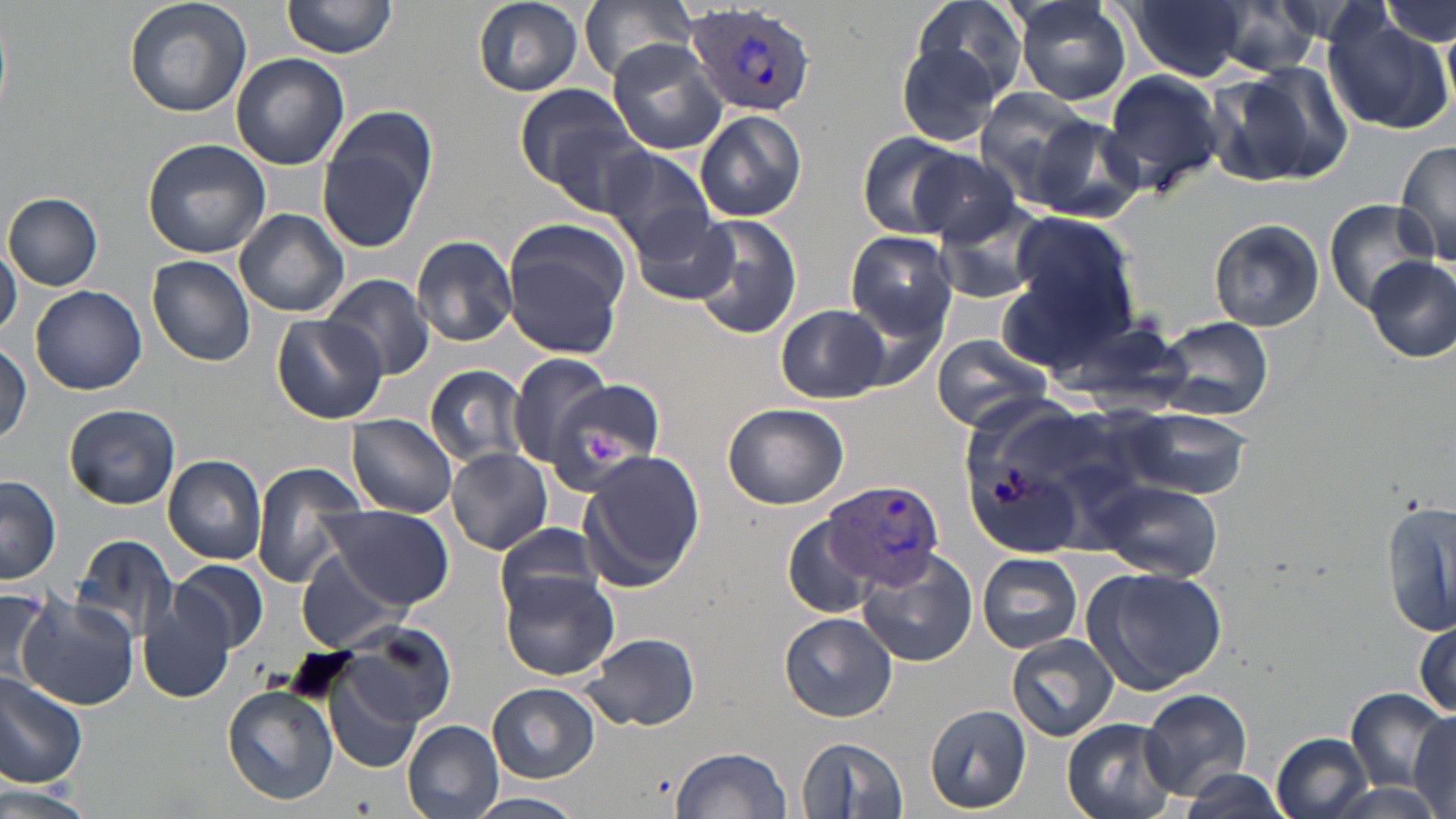

Approximate bounding boxes as [x1, y1, x2, y2] in pixels. Platelet locations: [585, 432, 620, 461]. Plasmodium vivax-infected red blood cell locations: [688, 3, 819, 115], [823, 480, 943, 591]. Uninfected red blood cell locations: [123, 0, 252, 117], [282, 0, 399, 59], [473, 0, 584, 95], [576, 0, 700, 85], [910, 0, 1030, 104], [1011, 0, 1132, 106], [1128, 0, 1246, 81], [1378, 0, 1455, 47], [1209, 1, 1332, 76], [1323, 16, 1454, 134], [893, 38, 1006, 149], [605, 40, 728, 156], [229, 54, 349, 171], [1210, 62, 1354, 188], [1098, 66, 1224, 197], [512, 82, 638, 191], [973, 86, 1101, 201], [695, 109, 808, 222], [1021, 112, 1146, 222], [315, 118, 435, 252], [547, 120, 659, 216], [856, 131, 967, 239], [143, 139, 272, 259], [1393, 139, 1456, 267], [602, 147, 717, 256], [909, 150, 1028, 246], [4, 192, 103, 290], [937, 197, 1052, 304], [1323, 199, 1439, 315], [233, 209, 349, 318], [631, 212, 738, 306], [1003, 212, 1142, 357], [690, 214, 802, 338], [1209, 219, 1324, 331], [503, 220, 630, 355], [846, 231, 957, 338], [410, 235, 519, 346], [0, 242, 21, 339], [147, 256, 258, 366], [1364, 256, 1456, 364], [323, 273, 436, 381], [31, 285, 147, 394], [777, 304, 887, 403], [1047, 309, 1193, 406], [270, 312, 388, 423], [1155, 317, 1274, 421], [928, 334, 1057, 431], [1, 343, 31, 451], [509, 353, 617, 467], [425, 365, 530, 468], [549, 382, 668, 486], [64, 402, 181, 510], [723, 402, 849, 509], [1112, 405, 1250, 498], [346, 414, 458, 518], [446, 447, 553, 557], [163, 454, 267, 565], [579, 454, 702, 591], [249, 463, 369, 587], [1, 475, 61, 583], [1091, 480, 1223, 580], [1384, 501, 1455, 638], [320, 504, 452, 607], [782, 516, 875, 620], [496, 522, 610, 618], [70, 536, 182, 644], [856, 547, 979, 667], [298, 549, 412, 653], [976, 552, 1083, 653], [171, 560, 268, 653], [1081, 565, 1228, 694], [501, 573, 619, 680], [0, 587, 56, 691], [17, 596, 140, 711], [139, 598, 234, 703], [779, 612, 897, 722], [1413, 618, 1455, 723], [340, 620, 455, 728], [581, 633, 701, 731], [1008, 634, 1119, 741], [0, 666, 89, 788], [323, 670, 426, 774], [487, 683, 598, 781], [223, 685, 339, 806], [1140, 688, 1254, 799], [1347, 690, 1447, 794], [924, 703, 1033, 814], [1410, 710, 1456, 815], [1062, 718, 1179, 819], [403, 720, 504, 818], [1271, 731, 1374, 818], [798, 736, 908, 817], [672, 746, 793, 819], [1173, 770, 1293, 818], [0, 783, 95, 819], [470, 792, 584, 819]. Slide-level diagnosis: Plasmodium vivax. Thin blood smear. 1000x magnification. May-Grünwald-Giemsa stain. Single field of view. Image is 1456×819 pixels. Light microscopy.